Comment on the morphology of the red blood cells.
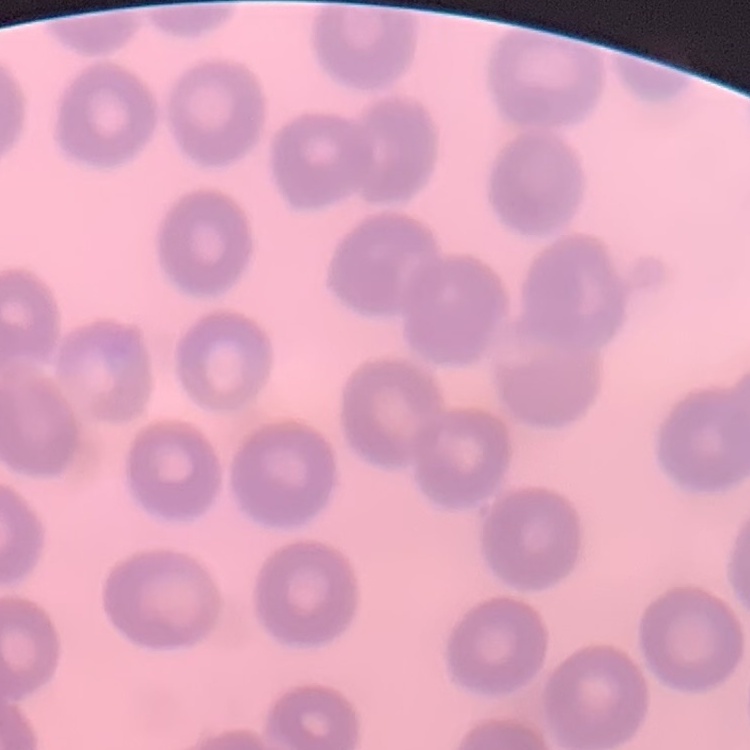

No rouleaux formation.

Summary:
  - Preparation: thin peripheral smear
  - Image type: one tile cut from a larger photomicrograph
  - Stain: Field's or Giemsa